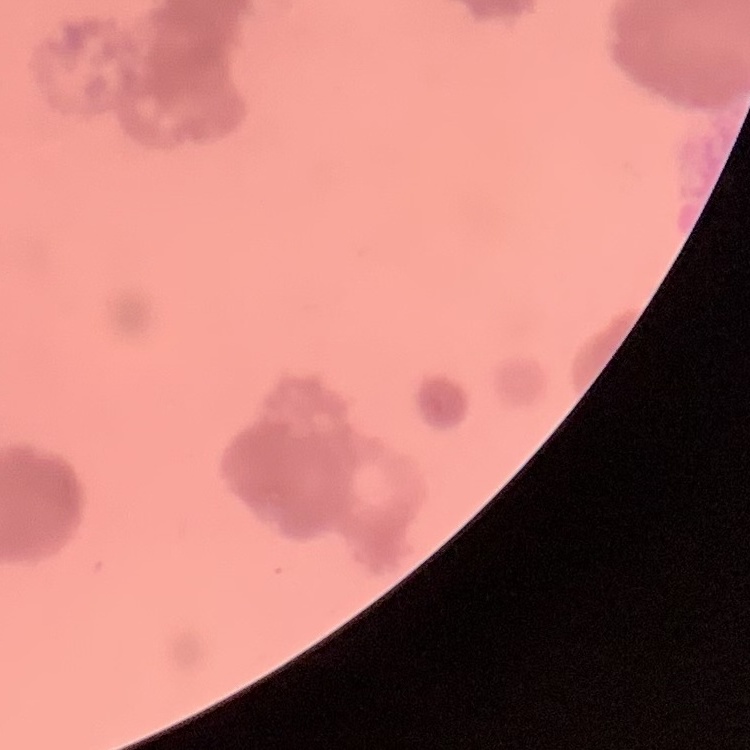

Summary:
  - Erythrocyte morphology: rouleaux formation
  - Image type: square crop of a larger photomicrograph
  - Preparation: thin blood smear
  - Stain: Field's or Giemsa